Classify this cell by malaria status.
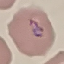
Parasitized.

Acquired by smartphone through the microscope eyepiece. Thin smear of blood. Automatically extracted cell patch, resized to 64 × 64 pixels. Giemsa-stained preparation.